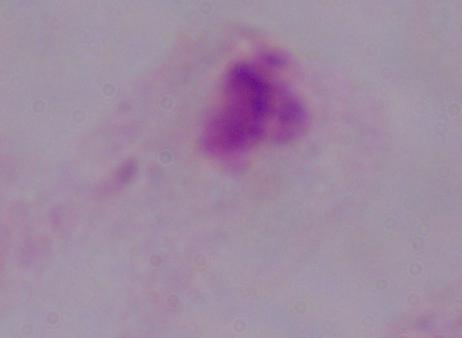
magnification = 1000x
modality = micrograph
identification = trichomonad